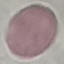

Summary:
  - Result: negative for malaria parasites
  - Stain: Giemsa
  - Preparation: thin smear
  - Capture: smartphone through the microscope eyepiece
  - Image type: automatically extracted cell patch, resized to 64 × 64 pixels